Locate every Plasmodium ovale-infected red blood cell.
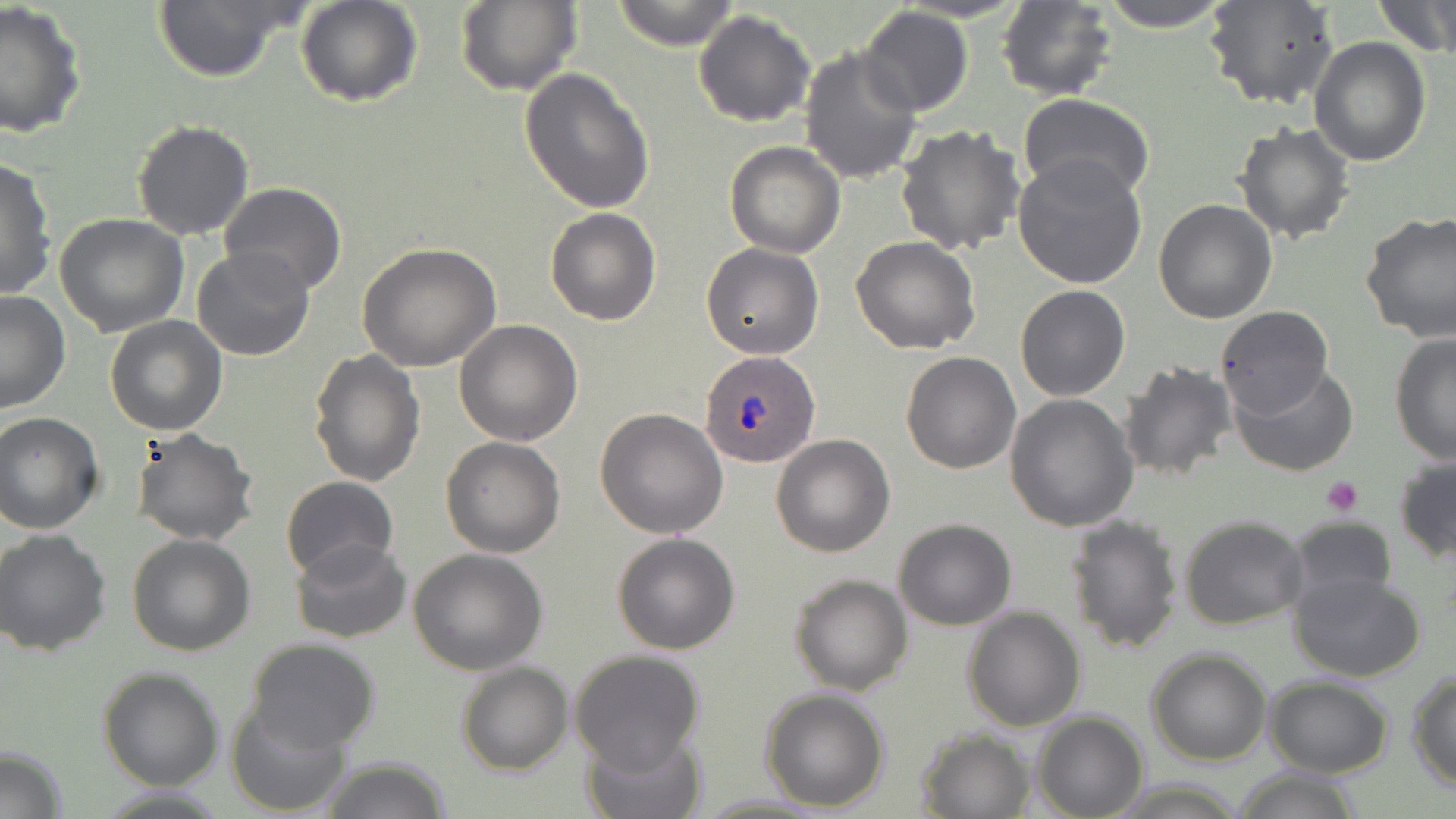

Approximate bounding boxes as [x1, y1, x2, y2] in pixels.
Plasmodium ovale-infected red blood cells: [696, 350, 821, 467].

Uninfected red blood cell locations: [149, 0, 304, 84], [294, 0, 423, 107], [456, 0, 582, 97], [608, 0, 742, 51], [1096, 0, 1233, 32], [1203, 0, 1339, 111], [1374, 0, 1455, 58], [996, 1, 1120, 101], [0, 3, 89, 138], [857, 6, 973, 117], [694, 11, 817, 127], [1309, 38, 1432, 168], [799, 45, 922, 184], [518, 67, 655, 215], [1019, 94, 1155, 204], [131, 120, 254, 241], [1234, 122, 1357, 244], [895, 124, 1025, 257], [724, 141, 846, 257], [1012, 154, 1148, 290], [0, 156, 56, 301], [219, 181, 347, 295], [1152, 199, 1277, 322], [545, 208, 661, 326], [1360, 211, 1456, 342], [53, 213, 190, 336], [851, 236, 981, 354], [357, 242, 503, 372], [701, 243, 825, 358], [191, 246, 316, 362], [1014, 284, 1131, 401], [0, 290, 71, 414], [1215, 305, 1332, 417], [105, 315, 227, 436], [454, 320, 584, 445], [1390, 330, 1456, 465], [310, 347, 425, 486], [900, 351, 1022, 474], [1117, 360, 1239, 483], [1231, 364, 1358, 476], [1005, 395, 1139, 531], [595, 408, 730, 538], [0, 412, 104, 534], [129, 428, 259, 547], [770, 434, 894, 557], [440, 436, 566, 556], [1395, 453, 1456, 564], [280, 475, 398, 580], [1064, 514, 1183, 654], [1179, 515, 1310, 628], [1285, 517, 1398, 613], [894, 518, 1016, 630], [0, 528, 111, 656], [612, 532, 740, 655], [127, 534, 256, 657], [289, 537, 411, 644], [407, 548, 550, 676], [1288, 568, 1426, 681], [789, 573, 912, 695], [961, 606, 1087, 732], [246, 638, 381, 752], [1146, 648, 1273, 766], [568, 649, 706, 773], [456, 661, 573, 775], [98, 668, 224, 791], [1406, 668, 1456, 792], [1264, 677, 1394, 777], [759, 688, 891, 811], [228, 700, 352, 817], [1032, 712, 1147, 818], [917, 727, 1035, 818], [581, 728, 704, 818], [0, 746, 67, 817], [319, 760, 449, 817], [1227, 769, 1366, 818]. Platelet locations: [1320, 476, 1365, 517]. Slide-level diagnosis: Plasmodium ovale. One field of a larger specimen. Optical microscopy. May-Grünwald-Giemsa-stained preparation. Captured at 1000x magnification. Thin blood smear. Image is 1456×819 pixels.